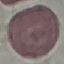

Summary:
  - Result: no malaria parasites seen
  - Stain: Giemsa
  - Image type: automatically extracted cell patch, resized to 64 × 64 pixels
  - Capture: smartphone through the microscope eyepiece
  - Preparation: thin blood smear